Report the malaria status of this cell.
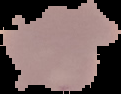
Uninfected.

Summary:
  - Image type: cell region segmented out of the field of view; surrounding area masked to black
  - Image size: 121×94 pixels
  - Preparation: thin blood film